Identify the preparation type.
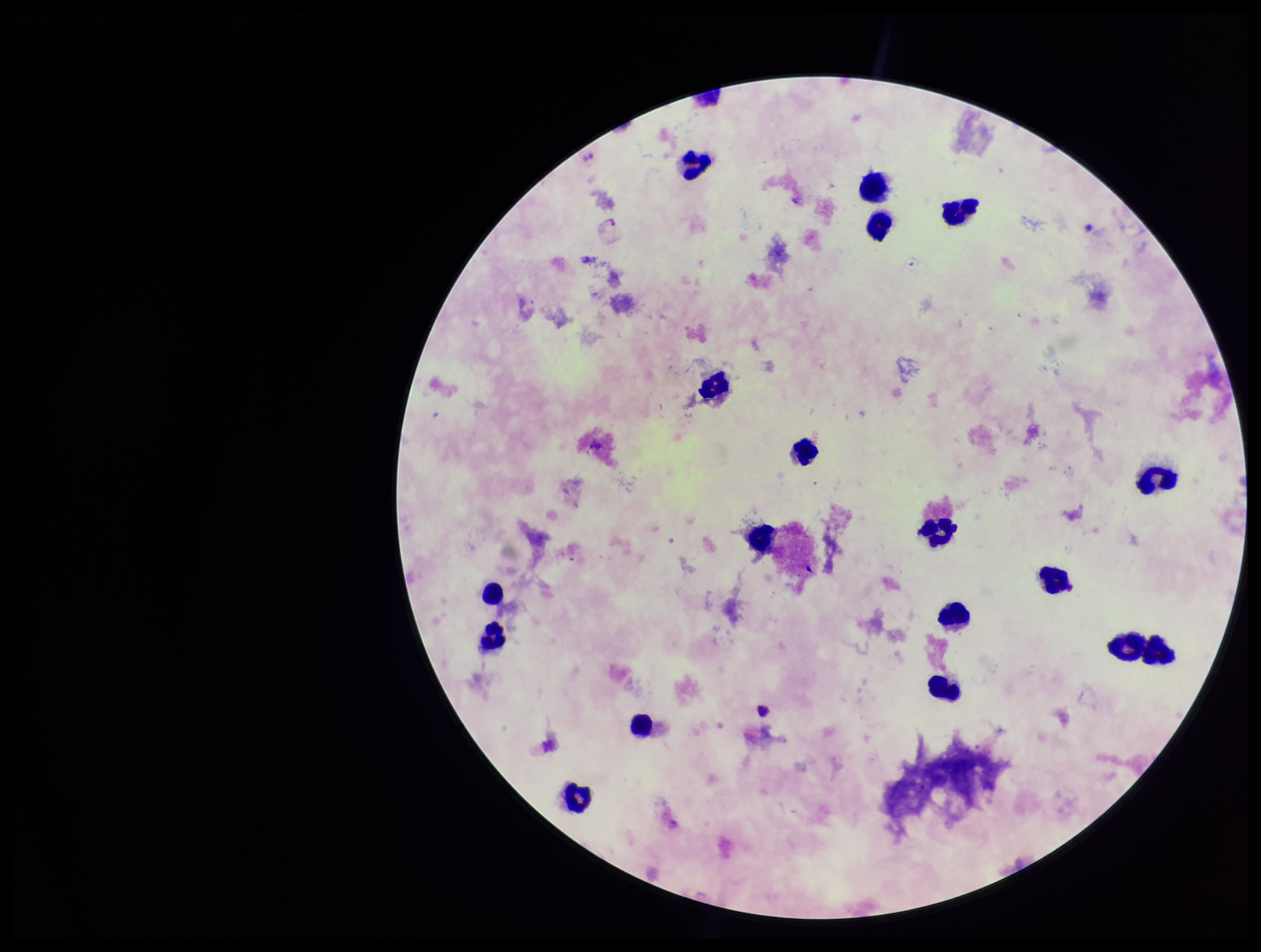
It is a thick blood smear.

Summary:
  - Stain: Giemsa
  - Parasite count: 2
  - Field of view: one from this slide
  - Capture: smartphone photograph through the microscope eyepiece
  - Image size: 1261×952 pixels
  - Species reported for this patient: Plasmodium vivax
  - Plasmodium parasites: identified
  - Patient malaria status: positive
  - Leukocyte count: 18